Name the blood parasite species.
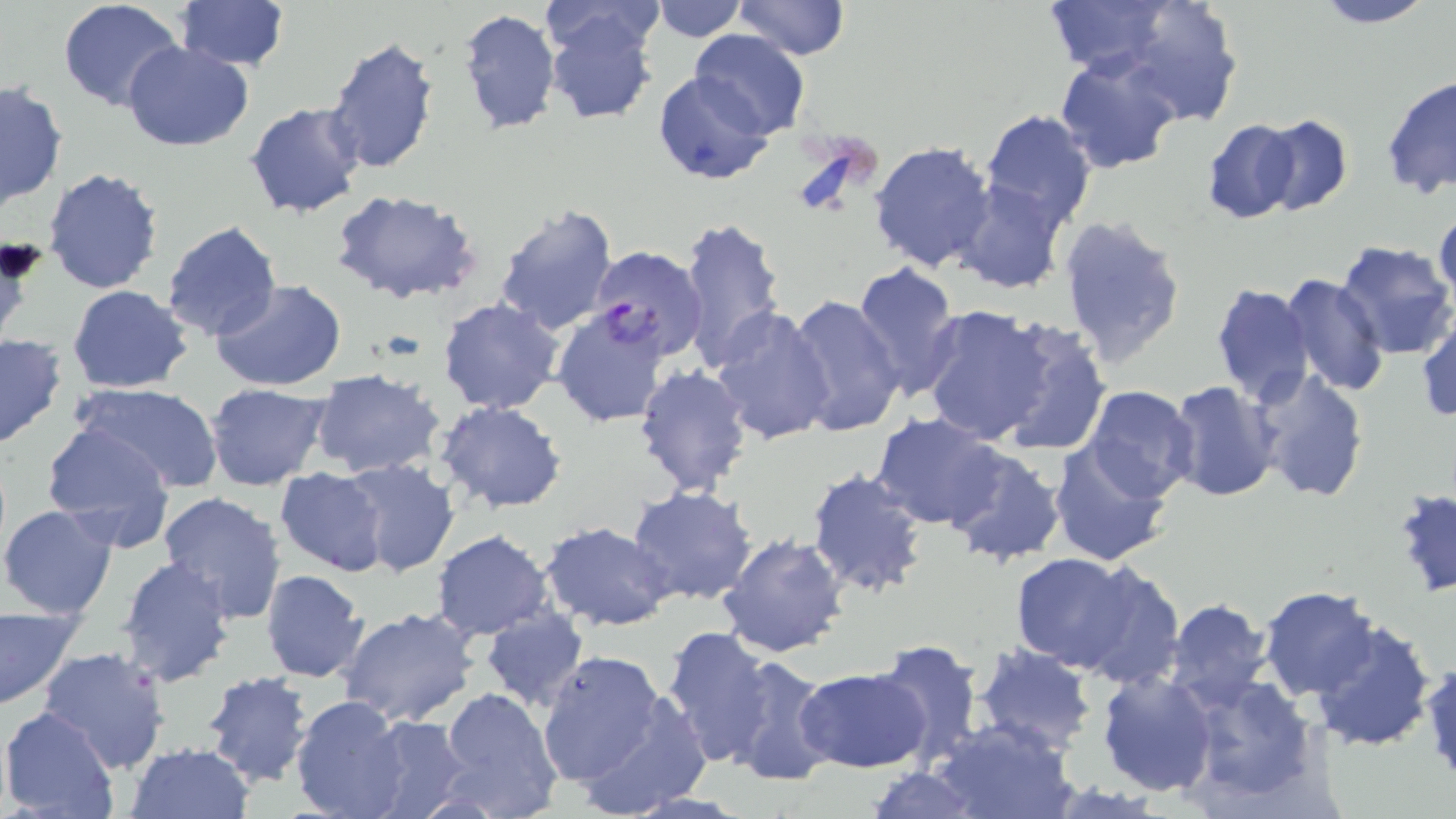
Plasmodium falciparum.

Approximate bounding boxes as (x1,y1)-(x2,y2) corner pairs in pixels. Plasmodium falciparum-infected red blood cell locations: (589,246)-(707,361). Uninfected red blood cell locations: (651,0)-(746,41), (734,0)-(850,61), (1040,0)-(1179,78), (1310,0)-(1438,28), (1110,1)-(1246,123), (57,2)-(185,113), (175,2)-(291,73), (540,2)-(668,61), (457,8)-(561,138), (546,11)-(658,126), (689,29)-(808,137), (324,35)-(440,174), (121,39)-(255,152), (1056,54)-(1180,175), (654,69)-(776,185), (1381,74)-(1456,199), (0,82)-(67,210), (244,101)-(367,219), (979,109)-(1097,235), (1257,114)-(1354,216), (1201,119)-(1301,223), (868,139)-(997,274), (41,166)-(165,295), (950,180)-(1067,294), (330,189)-(482,305), (492,201)-(621,337), (1433,210)-(1456,307), (677,214)-(786,371), (1055,214)-(1188,370), (160,220)-(282,343), (1334,241)-(1456,361), (850,262)-(962,401), (1280,271)-(1388,397), (212,280)-(345,390), (1211,283)-(1315,405), (68,284)-(193,392), (787,295)-(905,438), (438,298)-(565,417), (919,304)-(1057,444), (552,307)-(672,429), (711,307)-(838,447), (991,318)-(1111,458), (1416,319)-(1456,423), (0,333)-(68,450), (631,363)-(753,498), (1250,367)-(1368,504), (311,369)-(447,479), (71,381)-(225,494), (1165,381)-(1281,502), (204,382)-(332,489), (1083,385)-(1201,500), (435,401)-(568,514), (869,415)-(1009,530), (39,421)-(179,553), (1048,440)-(1173,567), (945,447)-(1066,567), (338,456)-(462,579), (274,465)-(389,577), (805,468)-(930,600), (626,486)-(758,608), (155,490)-(287,625), (0,504)-(120,620), (539,522)-(676,632), (432,530)-(555,640), (716,532)-(849,658), (1008,553)-(1147,672), (116,556)-(236,688), (1071,562)-(1185,688), (260,569)-(370,684), (1259,586)-(1382,700), (1163,599)-(1275,713), (0,604)-(82,708), (335,606)-(482,728), (480,609)-(588,712), (1309,618)-(1438,753), (661,626)-(775,769), (870,639)-(985,766), (972,645)-(1098,753), (37,646)-(171,773), (536,649)-(674,799), (723,655)-(835,788), (1422,655)-(1455,787), (795,667)-(930,773), (1098,670)-(1217,796), (201,671)-(317,788), (1182,675)-(1323,808), (434,686)-(563,818), (564,686)-(714,818), (289,694)-(413,819), (1,706)-(121,817), (364,716)-(475,819), (931,716)-(1079,819), (125,741)-(254,818), (864,764)-(982,819). Captured at 1000x magnification. Single field of view. Light microscopy. Image is 1456×819 pixels. May-Grünwald-Giemsa-stained preparation. Thin blood film.